Evaluate for malaria.
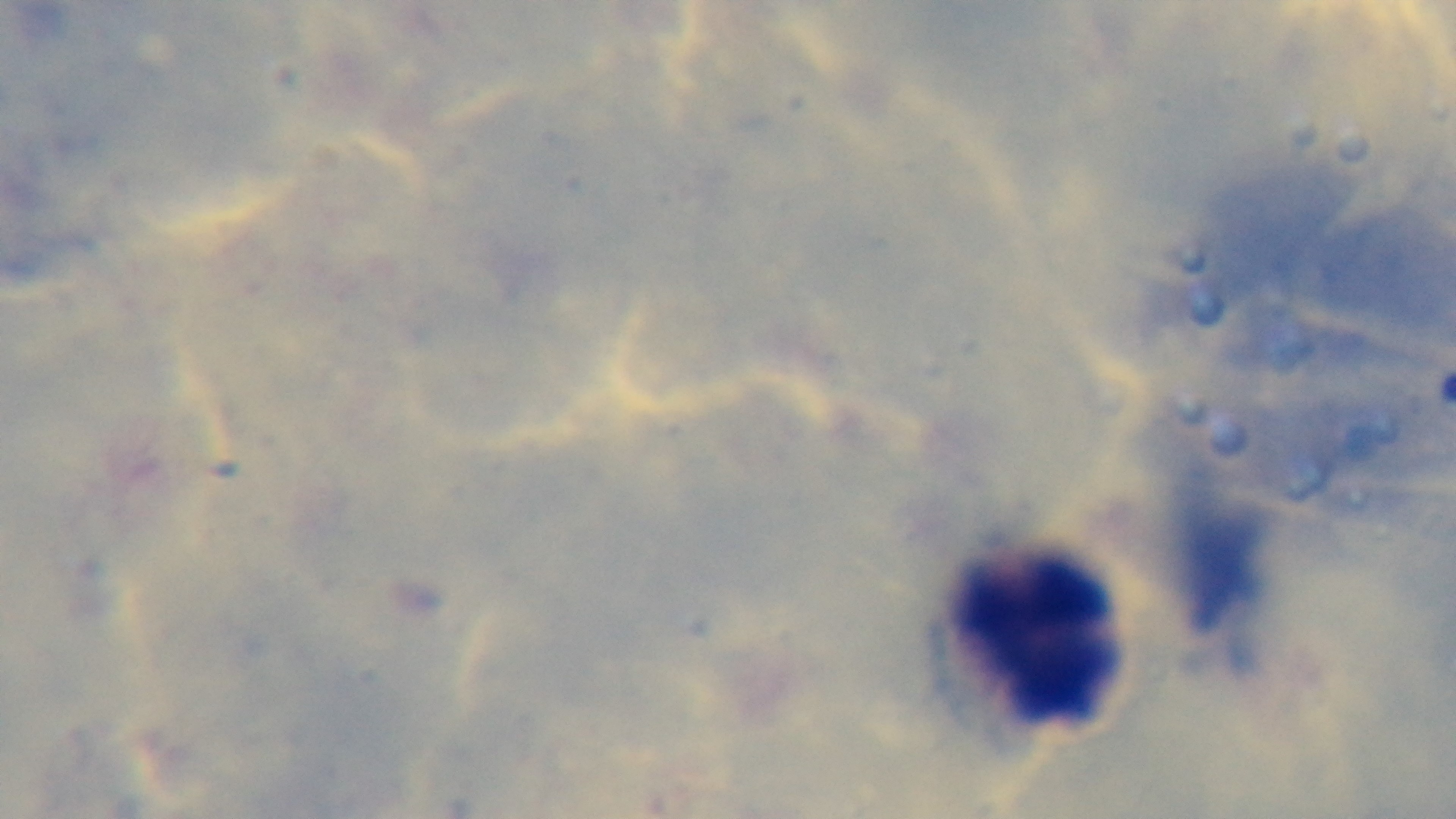

Negative.

Summary:
  - Capture: mounted 4K digital camera
  - Stain: Giemsa
  - Objective: 100x oil immersion
  - Modality: light microscopy
  - Field of view: one from the slide
  - Preparation: thick smear